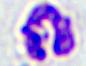 A white blood cell is seen. Micrograph. Captured at 400x magnification.